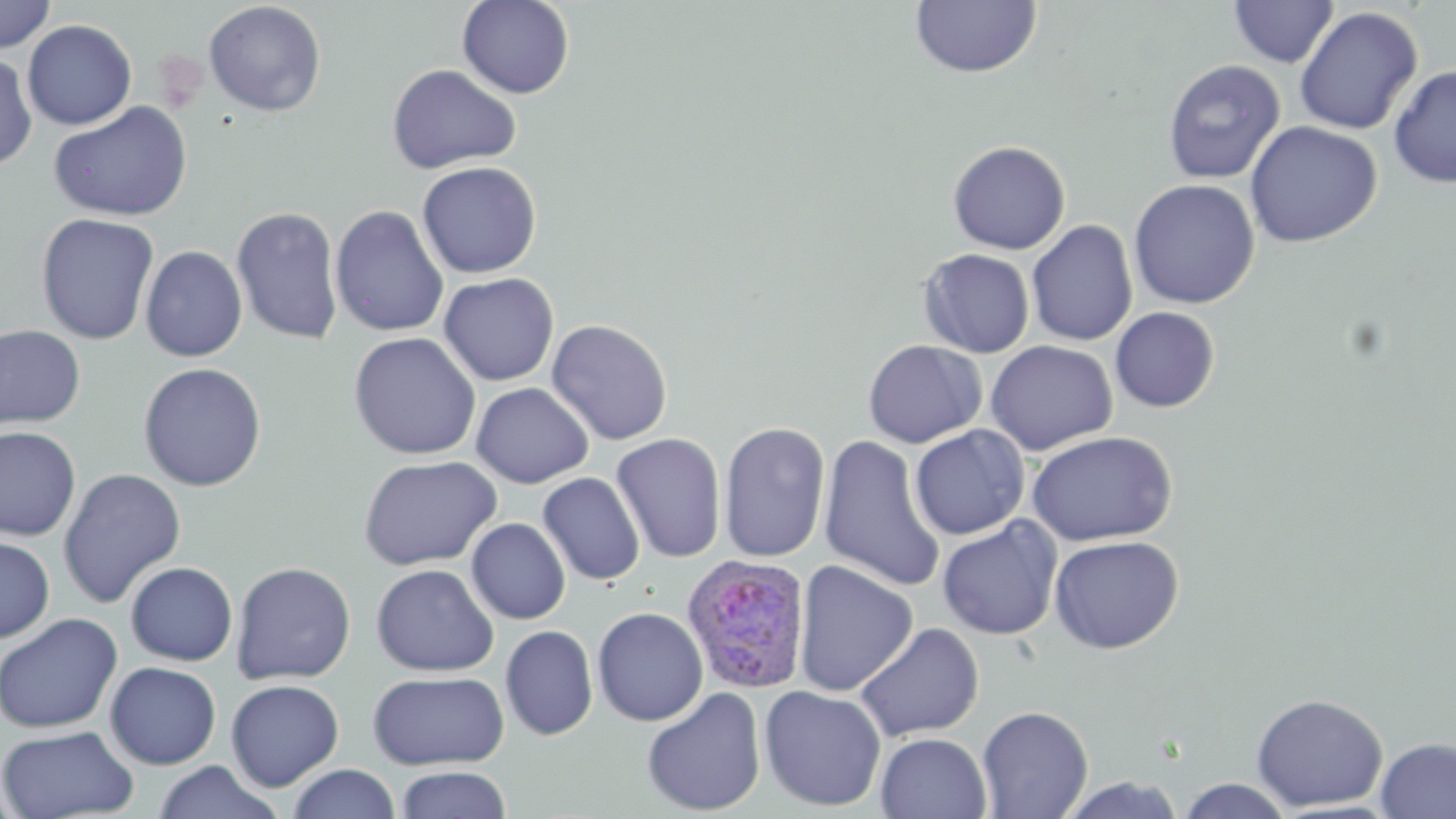
Summary:
  - Coordinate format: approximate bounding boxes as (x1,y1)-(x2,y2) corner pairs in pixels
  - Plasmodium ovale-infected red blood cell locations: (680,553)-(812,693)
  - Uninfected red blood cell locations: (0,0)-(57,54), (457,0)-(575,99), (1229,0)-(1339,67), (203,1)-(327,117), (910,1)-(1042,79), (1294,6)-(1423,135), (22,19)-(137,130), (0,51)-(38,172), (1162,59)-(1286,183), (386,63)-(522,175), (1387,64)-(1456,188), (48,100)-(194,222), (1245,120)-(1383,248), (947,140)-(1071,255), (416,161)-(542,279), (1129,178)-(1260,309), (330,204)-(449,338), (232,205)-(344,345), (35,212)-(160,345), (1026,220)-(1138,346), (140,245)-(248,362), (918,248)-(1035,358), (438,272)-(560,386), (1110,307)-(1220,412), (546,318)-(673,446), (0,324)-(86,430), (348,332)-(482,460), (863,339)-(987,448), (986,340)-(1118,455), (138,362)-(267,492), (470,382)-(593,488), (718,421)-(830,563), (909,425)-(1030,540), (0,426)-(81,541), (1026,431)-(1178,546), (611,432)-(727,563), (818,434)-(946,592), (358,455)-(502,571), (58,468)-(186,609), (537,472)-(645,586), (937,517)-(1062,639), (467,518)-(570,624), (1048,534)-(1184,654), (0,535)-(55,643), (793,560)-(919,697), (125,561)-(238,666), (230,561)-(356,685), (371,563)-(500,676), (592,606)-(709,726), (0,613)-(123,734), (855,622)-(984,742), (500,625)-(598,740), (104,661)-(221,769), (367,670)-(510,770), (226,679)-(344,790), (758,685)-(887,811), (642,687)-(766,816), (1251,693)-(1388,812), (977,705)-(1093,818), (0,724)-(139,818), (875,732)-(992,819), (1374,736)-(1456,819), (152,761)-(284,819), (286,763)-(402,819), (394,766)-(513,818), (1058,775)-(1188,818), (1176,778)-(1295,818), (0,779)-(24,819)
  - Slide-level diagnosis: Plasmodium ovale
  - Magnification: 1000x
  - Preparation: thin blood smear
  - Field of view: single
  - Stain: May-Grünwald-Giemsa
  - Image size: 1456×819 pixels
  - Modality: optical microscopy